Identify the blood parasite species.
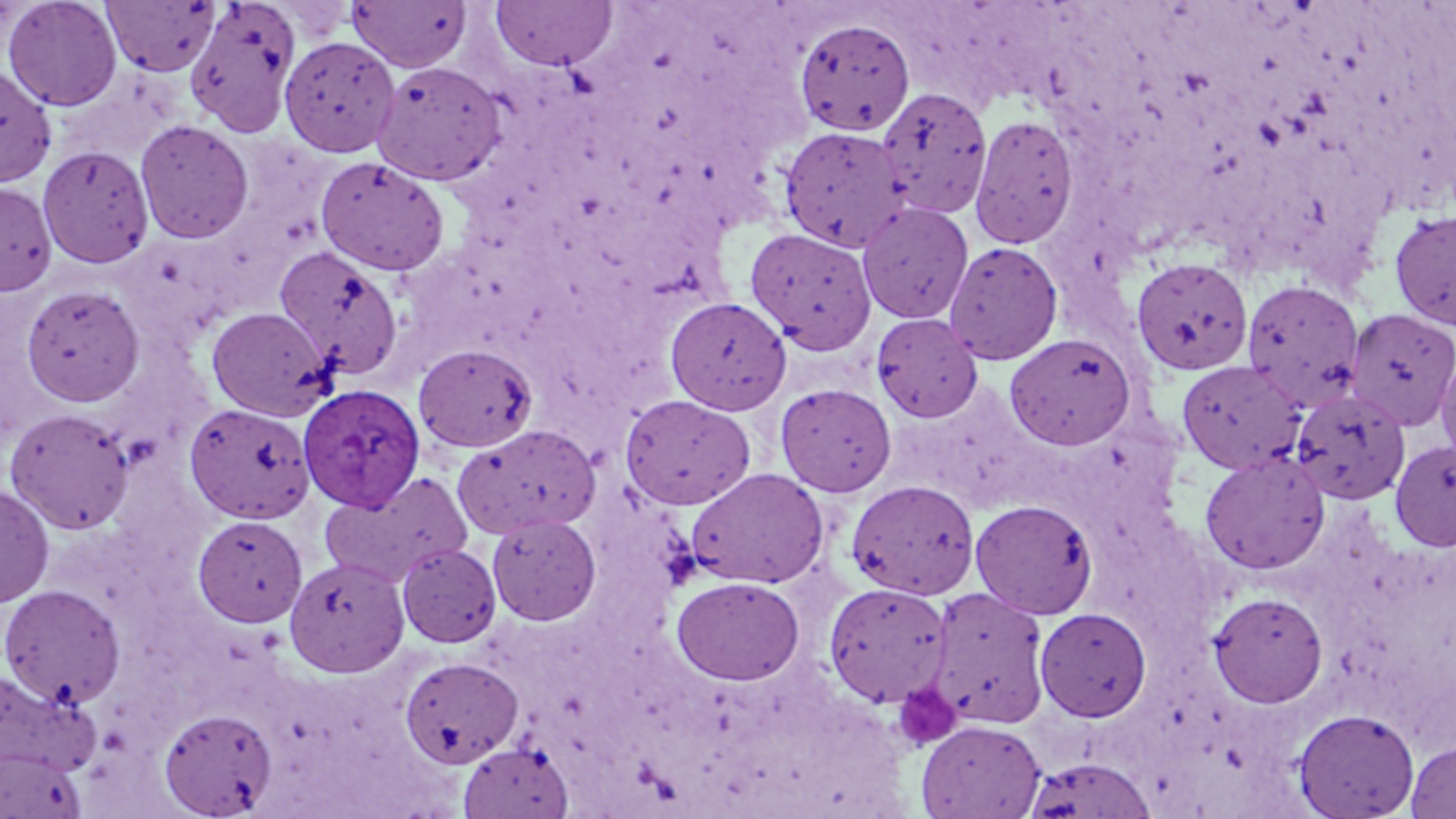
Plasmodium vivax.

Summary:
  - Coordinate format: approximate bounding boxes as (x1, y1, x2, y2) in pixels
  - Plasmodium vivax-infected red blood cell locations: (298, 384, 425, 513)
  - Platelet locations: (892, 680, 961, 751)
  - Uninfected red blood cell locations: (2, 0, 122, 111), (491, 0, 617, 71), (103, 1, 220, 76), (347, 1, 473, 72), (185, 2, 301, 138), (794, 18, 916, 138), (279, 35, 400, 157), (372, 60, 505, 185), (0, 63, 57, 185), (874, 86, 994, 218), (969, 114, 1080, 250), (135, 119, 254, 244), (779, 125, 912, 252), (38, 145, 154, 268), (315, 156, 450, 275), (0, 181, 57, 296), (857, 202, 975, 324), (1389, 209, 1456, 331), (745, 227, 878, 354), (943, 241, 1064, 364), (272, 245, 406, 381), (1132, 257, 1253, 376), (1241, 278, 1365, 410), (21, 285, 144, 406), (665, 296, 791, 414), (205, 306, 335, 421), (1346, 308, 1456, 431), (870, 313, 984, 423), (1004, 333, 1136, 450), (413, 343, 538, 453), (1435, 351, 1456, 473), (1176, 359, 1307, 474), (775, 383, 897, 497), (1291, 389, 1412, 504), (619, 394, 756, 510), (184, 402, 316, 524), (4, 407, 136, 535), (454, 424, 601, 539), (1390, 439, 1456, 551), (1199, 450, 1331, 575), (686, 468, 829, 589), (320, 472, 473, 587), (847, 480, 980, 599), (0, 483, 55, 608), (970, 500, 1098, 619), (486, 513, 602, 625), (192, 514, 307, 627), (397, 542, 502, 648), (284, 556, 409, 677), (672, 576, 805, 685), (823, 582, 952, 707), (0, 583, 126, 707), (925, 586, 1051, 731), (1208, 592, 1329, 708), (1034, 607, 1152, 722), (400, 656, 523, 768), (0, 668, 101, 788), (158, 707, 278, 818), (1294, 708, 1420, 818), (916, 719, 1046, 819), (1404, 738, 1456, 819), (459, 741, 575, 819), (0, 747, 88, 818), (1021, 756, 1159, 818)
  - Preparation: thin blood smear
  - Magnification: 1000x
  - Image size: 1456×819 pixels
  - Stain: May-Grünwald-Giemsa
  - Field of view: one of a larger specimen
  - Modality: optical microscopy